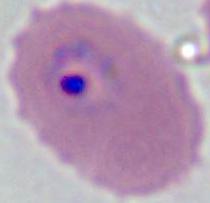
{
  "identification": "Plasmodium",
  "modality": "photomicrograph",
  "magnification": "400x or 1000x"
}